Report the malaria status of this cell.
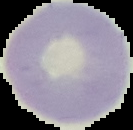
Uninfected.

image type = segmented cell region with the area outside set to black
preparation = thin blood smear
image size = 133×130 pixels